Comment on the morphology of the erythrocytes.
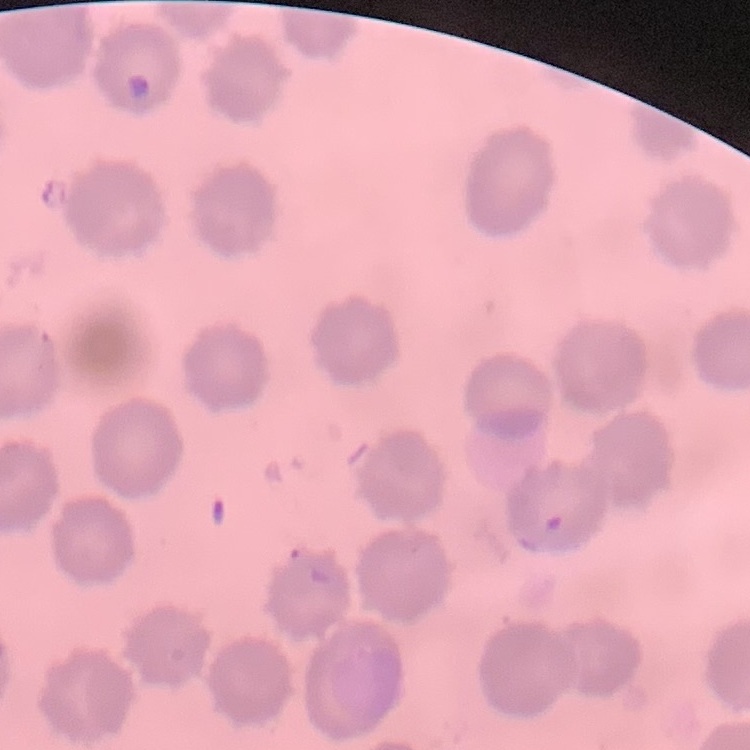
No rouleaux formation.

Summary:
  - Image type: square crop of a larger photomicrograph
  - Stain: Field's or Giemsa
  - Preparation: thin peripheral smear